Classify this cell by malaria status.
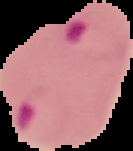

Parasitized.

preparation: thin blood smear
image_type: segmented cell region with the area outside set to black
image_size: 133×151 pixels